Classify this cell by malaria status.
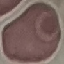

It is uninfected.

Giemsa-stained preparation. Thin blood film. Cell patch, automatically extracted from a larger field of view and resized to 64 × 64 pixels. Acquired by smartphone through the microscope eyepiece.